State the preparation type.
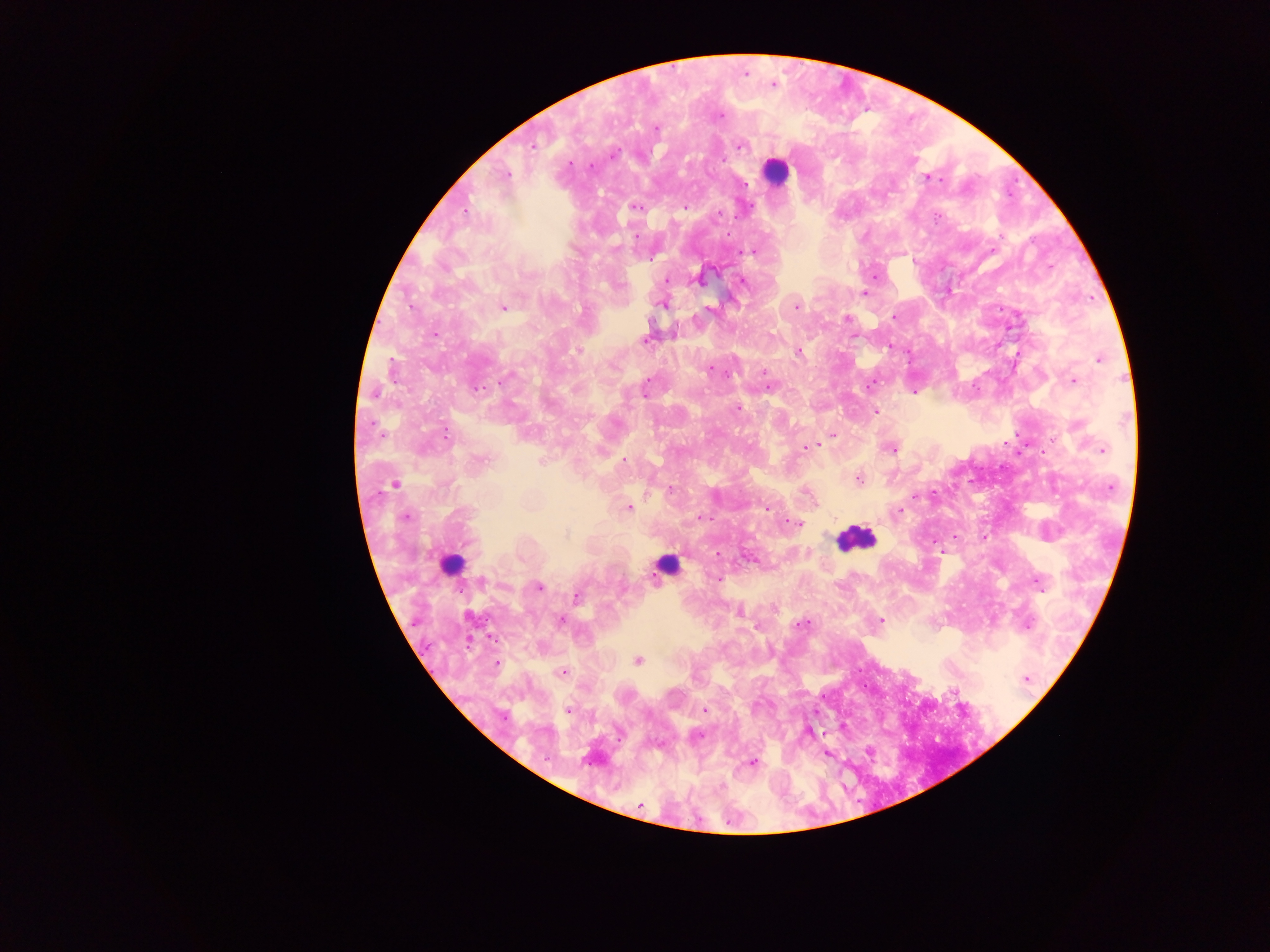

This is a thick smear.

capture = mobile-phone photograph through a microscope
country = Ghana
malaria parasite locations = approximate centers as {x, y} in pixels: {774, 85}, {720, 116}, {656, 128}, {534, 146}, {740, 146}, {614, 155}, {570, 164}, {590, 166}, {507, 174}, {928, 177}, {934, 179}, {745, 184}, {636, 207}, {684, 208}, {466, 209}, {719, 215}, {937, 217}, {636, 236}, {616, 248}, {752, 252}, {652, 258}, {666, 280}, {699, 280}, {743, 282}, {863, 293}, {662, 304}, {411, 307}, {503, 307}, {795, 307}, {709, 309}, {894, 316}, {848, 318}, {435, 334}, {645, 339}, {578, 350}, {798, 352}, {1099, 360}, {710, 369}, {763, 372}, {509, 376}, {647, 381}, {1073, 381}, {869, 385}, {767, 386}, {478, 388}, {645, 394}, {738, 409}, {875, 412}, {446, 435}, {833, 435}, {806, 447}, {891, 449}, {1102, 450}, {482, 460}, {624, 460}, {541, 461}, {858, 479}, {395, 484}, {1111, 486}, {671, 490}, {917, 495}, {628, 507}, {767, 509}, {899, 510}, {406, 516}, {700, 518}, {796, 523}, {565, 535}, {718, 579}, {482, 581}, {1039, 582}, {538, 587}, {577, 597}, {739, 613}, {561, 620}, {881, 620}, {801, 625}, {1028, 626}, {638, 660}, {497, 664}, {562, 671}, {1025, 679}, {568, 710}, {705, 710}, {699, 736}, {752, 762}, {640, 805}
field of view = single
image size = 1270×952 pixels
leukocyte locations = approximate centers as {x, y} in pixels: {775, 171}, {855, 538}, {450, 563}, {665, 564}